Classify this cell by malaria status.
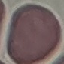
It is uninfected.

Summary:
  - Capture: smartphone camera at the microscope eyepiece
  - Preparation: thin smear
  - Stain: Giemsa
  - Image type: automatically extracted cell patch, resized to 64 × 64 pixels